Identify the preparation type.
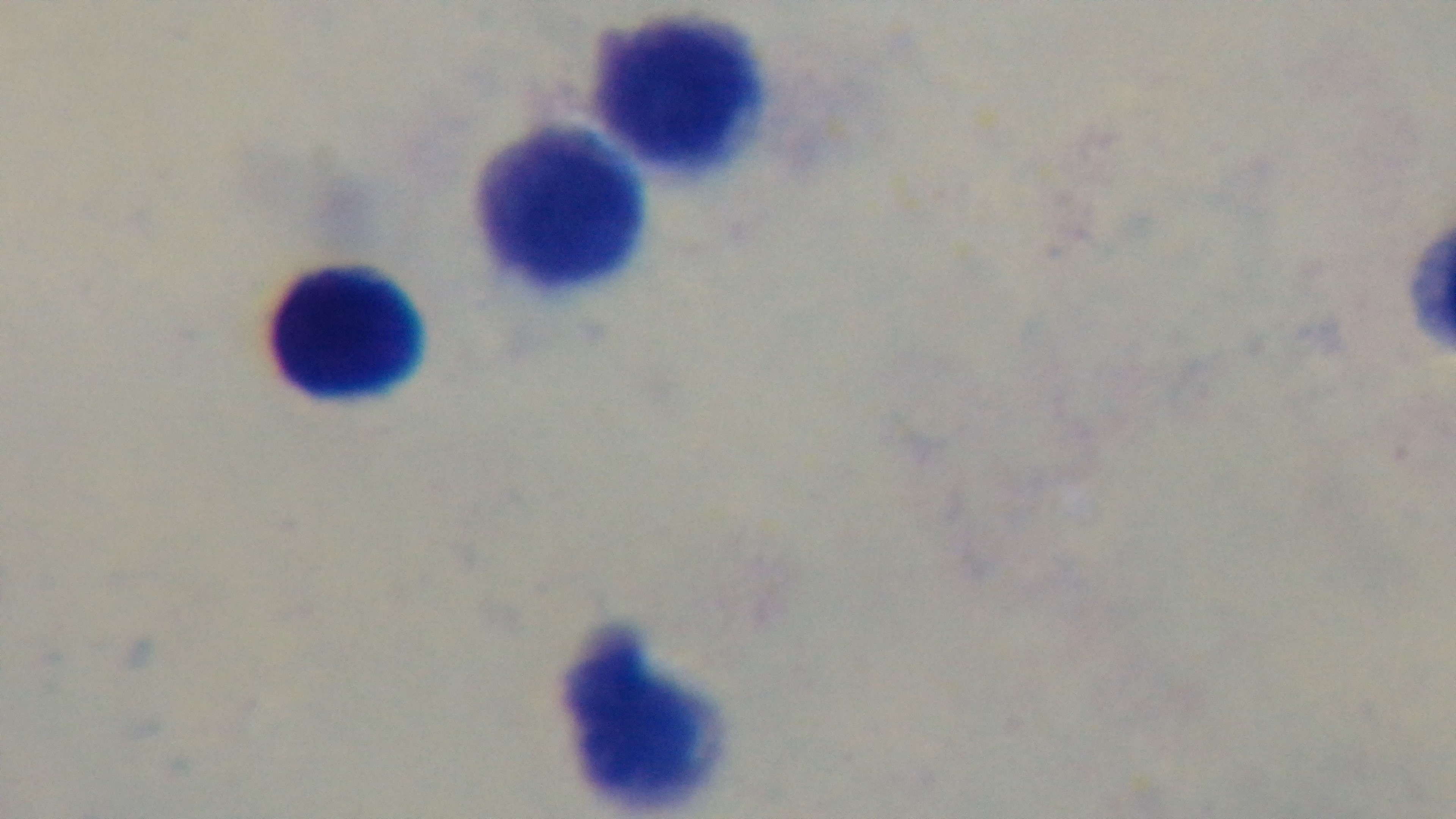
Thick.

malaria status = uninfected
modality = light microscopy
objective = 100x oil immersion
field of view = one from the slide
stain = Giemsa
capture = mounted 4K digital camera